Report the malaria status of this cell.
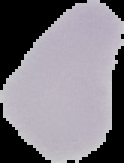

Uninfected.

From a thin blood smear. Segmented cell region on a black background. Image is 124×163 pixels.